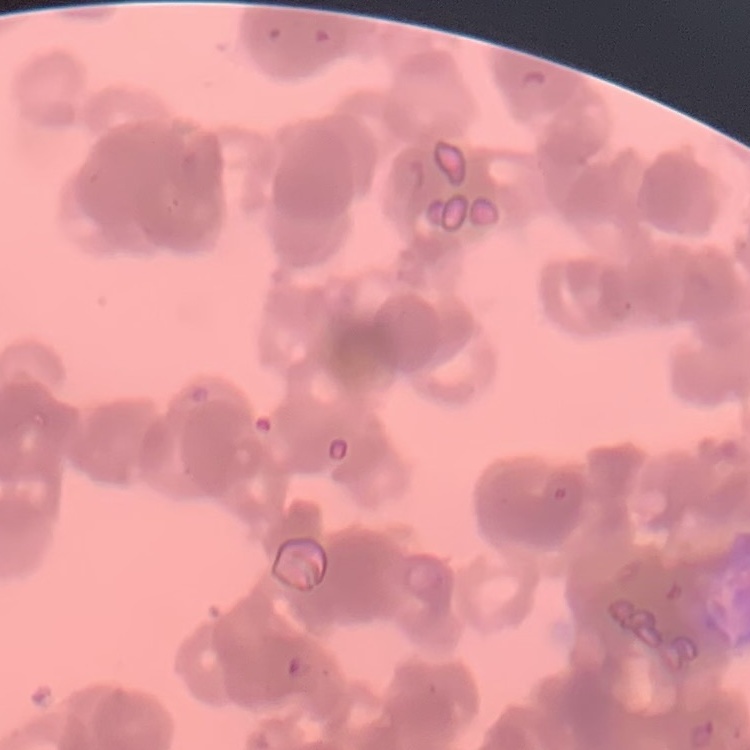

The erythrocytes show rouleaux formation. One tile cut from a larger photomicrograph. Thin peripheral smear. Field's or Giemsa stain.